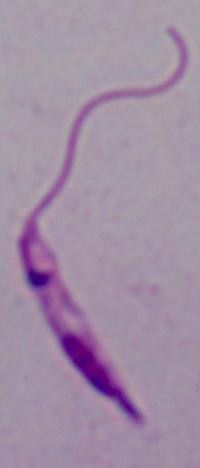
Captured at 1000x magnification. Micrograph. A Leishmania parasite is seen.